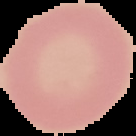 Image is 136×136 pixels. Malaria status: uninfected. From a thin blood smear. The area outside the segmented cell region is set to black.